Name the blood parasite species.
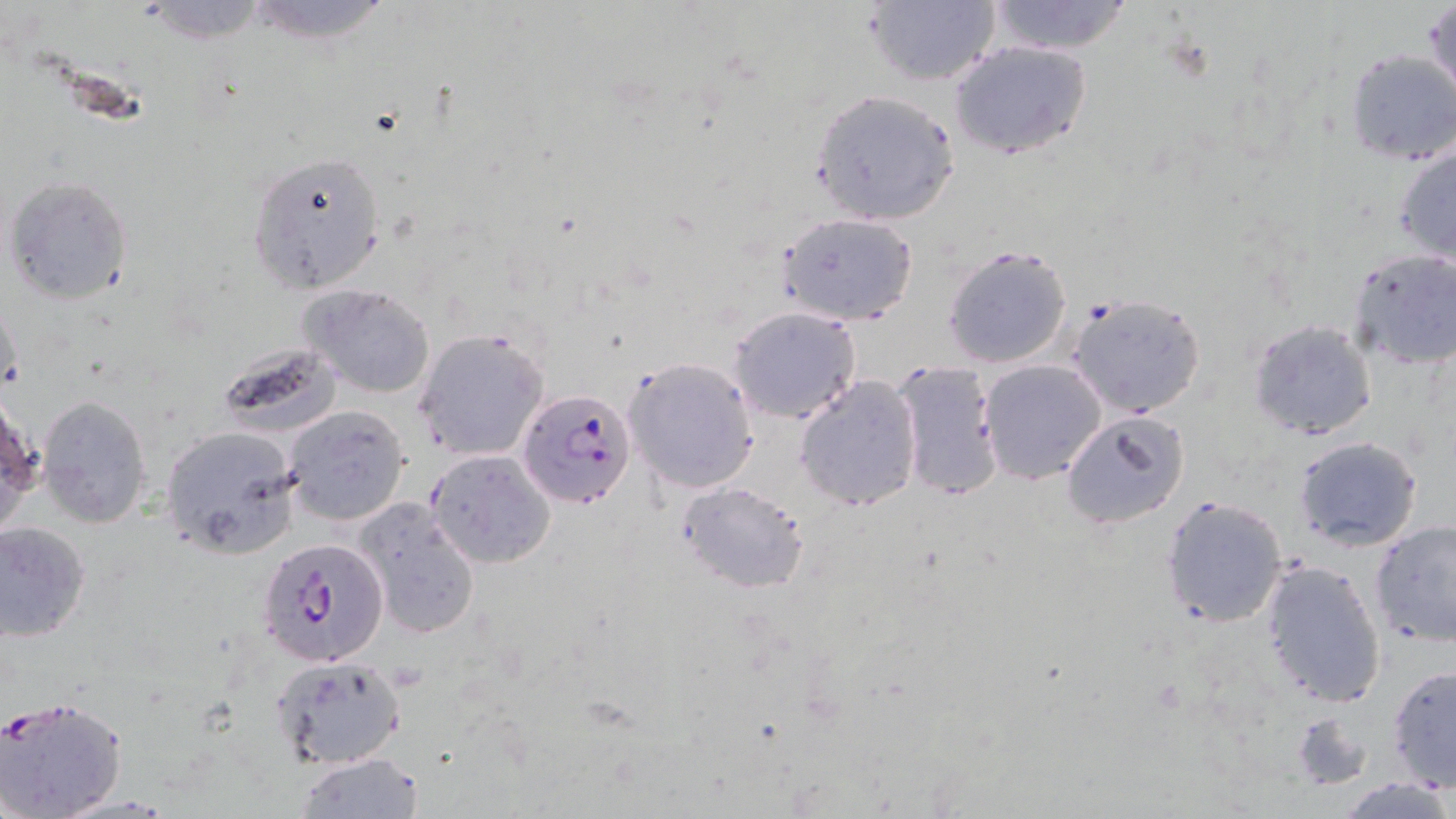
Plasmodium falciparum.

Approximate bounding boxes as [x1, y1, x2, y2] in pixels. Plasmodium falciparum-infected red blood cell locations: [516, 388, 638, 509], [257, 539, 387, 666], [0, 692, 128, 819]. Uninfected red blood cell locations: [235, 0, 399, 45], [1426, 0, 1456, 107], [863, 1, 1002, 88], [984, 1, 1134, 55], [949, 41, 1091, 160], [1342, 49, 1456, 166], [810, 89, 961, 226], [1392, 140, 1456, 269], [247, 150, 387, 295], [4, 175, 134, 306], [778, 213, 919, 325], [941, 243, 1075, 370], [1346, 249, 1456, 372], [300, 282, 436, 398], [0, 292, 22, 407], [1067, 293, 1206, 420], [727, 305, 862, 424], [1260, 318, 1392, 549], [1247, 320, 1378, 441], [414, 328, 551, 462], [215, 340, 345, 437], [894, 357, 1005, 503], [623, 358, 760, 494], [978, 359, 1108, 484], [794, 375, 924, 513], [38, 395, 154, 527], [283, 405, 410, 526], [1060, 408, 1189, 530], [159, 426, 300, 559], [1292, 435, 1424, 553], [426, 450, 556, 569], [678, 481, 812, 595], [1160, 494, 1289, 628], [356, 502, 482, 640], [1370, 519, 1456, 647], [0, 521, 90, 641], [1260, 559, 1387, 706], [270, 653, 408, 770], [1387, 664, 1456, 791], [1290, 711, 1374, 792], [294, 753, 424, 818], [1338, 776, 1454, 817]. Light microscopy. Image is 1456×819 pixels. Thin blood film. 1000x magnification. Single field of view. May-Grünwald-Giemsa-stained preparation.